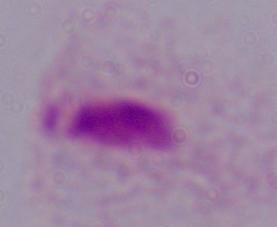 A trichomonad is shown. Captured at 1000x magnification. Micrograph.